State which parasite is depicted.
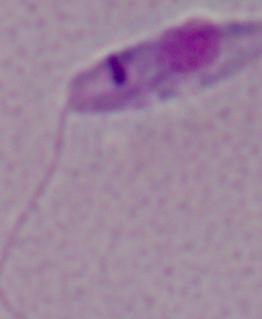
Leishmania.

Micrograph. 1000x magnification.